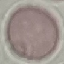
Summary:
  - Result: no malaria parasites detected
  - Preparation: thin smear
  - Image type: cell patch, automatically extracted from a larger field of view and resized to 64 × 64 pixels
  - Stain: Giemsa
  - Capture: smartphone camera at the microscope eyepiece